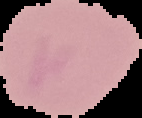
result = no Plasmodium parasites detected
preparation = thin blood smear
image type = cell region segmented out of the field of view; surrounding area masked to black
image size = 142×118 pixels